Report the malaria status of this cell.
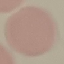
It is uninfected.

Automatically extracted cell patch, resized to 64 × 64 pixels. Giemsa stain. Thin blood film. Acquired by smartphone through the microscope eyepiece.